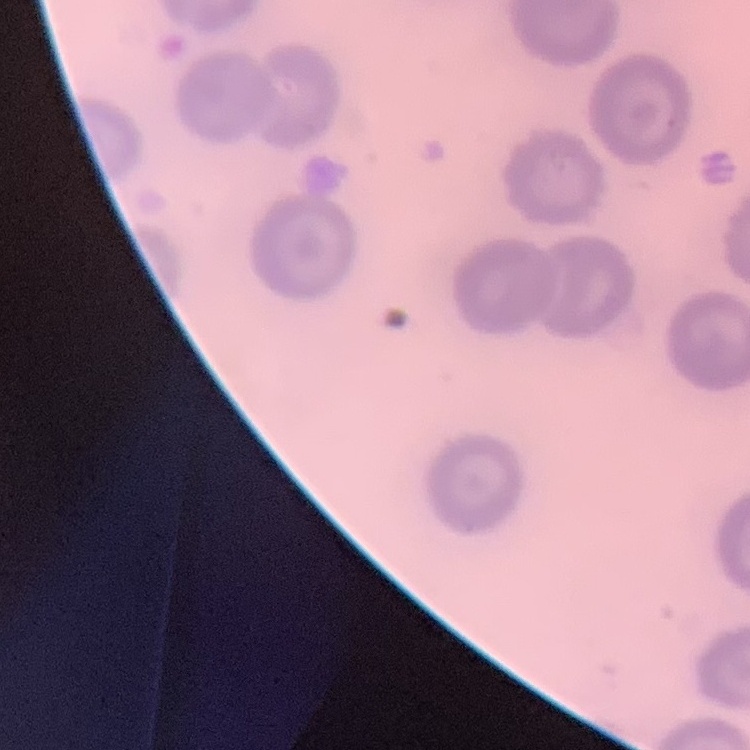

The erythrocytes show no rouleaux formation. Field's or Giemsa stain. Square crop of a larger photomicrograph. Thin blood film.